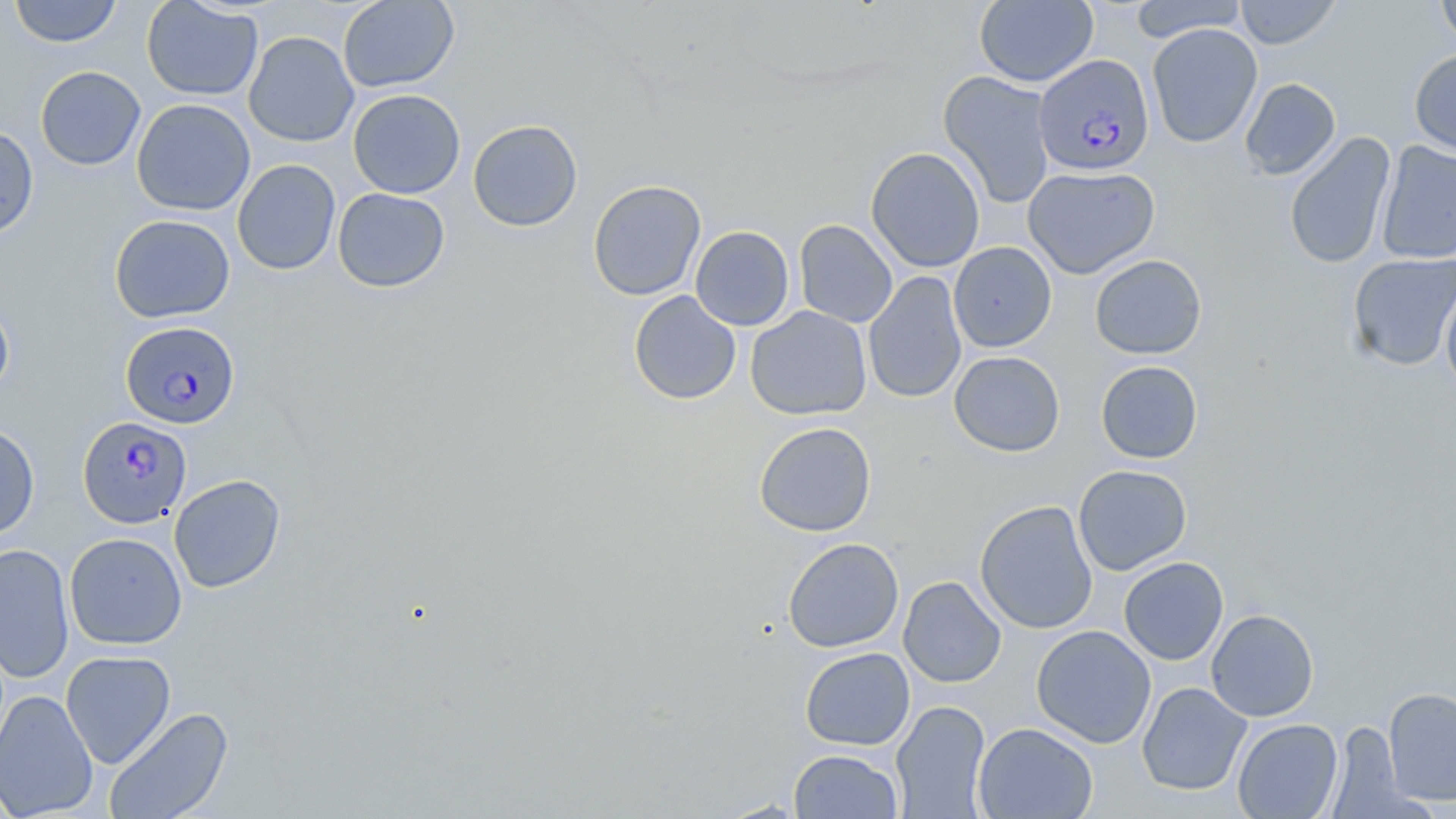

{
  "slide_level_diagnosis": "Plasmodium falciparum",
  "preparation": "thin blood film",
  "modality": "light microscopy",
  "magnification": "1000x",
  "uninfected_red_blood_cell_locations": "approximate bounding boxes as [x1, y1, x2, y2] in pixels: [9, 0, 123, 47], [141, 0, 263, 101], [974, 0, 1098, 88], [1128, 0, 1248, 42], [1233, 0, 1342, 49], [1435, 0, 1456, 53], [338, 1, 459, 92], [1147, 23, 1263, 148], [243, 31, 359, 147], [1409, 49, 1456, 157], [35, 66, 146, 170], [938, 70, 1056, 210], [1239, 78, 1341, 180], [348, 89, 465, 199], [131, 98, 255, 216], [468, 119, 583, 232], [0, 125, 39, 238], [1283, 131, 1396, 269], [1375, 141, 1456, 265], [865, 146, 986, 273], [232, 159, 341, 276], [1022, 166, 1159, 279], [588, 179, 706, 301], [333, 188, 450, 292], [109, 214, 235, 323], [794, 219, 898, 328], [690, 226, 795, 330], [949, 242, 1057, 352], [1347, 252, 1456, 371], [1089, 254, 1207, 359], [863, 271, 968, 404], [1440, 283, 1456, 399], [628, 290, 741, 405], [0, 296, 14, 402], [744, 305, 872, 421], [949, 350, 1065, 457], [1096, 360, 1203, 464], [753, 422, 877, 536], [0, 423, 40, 540], [1073, 465, 1192, 575], [168, 474, 286, 593], [974, 500, 1098, 634], [64, 532, 187, 650], [782, 538, 904, 653], [0, 542, 75, 683], [1118, 557, 1228, 665], [898, 576, 1006, 688], [1206, 608, 1319, 721], [1031, 625, 1157, 748], [800, 647, 915, 750], [60, 650, 176, 769], [1137, 682, 1252, 796], [1383, 686, 1456, 805], [0, 689, 98, 818], [891, 700, 992, 818], [103, 706, 234, 819], [1232, 718, 1343, 818], [973, 722, 1098, 819], [1329, 722, 1415, 818], [789, 749, 903, 818]",
  "plasmodium_falciparum_infected_red_blood_cell_locations": "approximate bounding boxes as [x1, y1, x2, y2] in pixels: [1034, 54, 1154, 176], [120, 320, 240, 429], [77, 416, 192, 529]",
  "field_of_view": "one of a larger specimen",
  "image_size": "1456×819 pixels",
  "stain": "May-Grünwald-Giemsa"
}